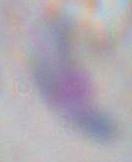 Toxoplasma gondii is shown. Captured at 1000x magnification. Photomicrograph.